Assess this cell for malaria.
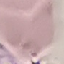
It is uninfected.

Acquired by smartphone through the microscope eyepiece. Giemsa stain. Cell patch, automatically extracted from a larger field of view and resized to 64 × 64 pixels. Thin blood smear.